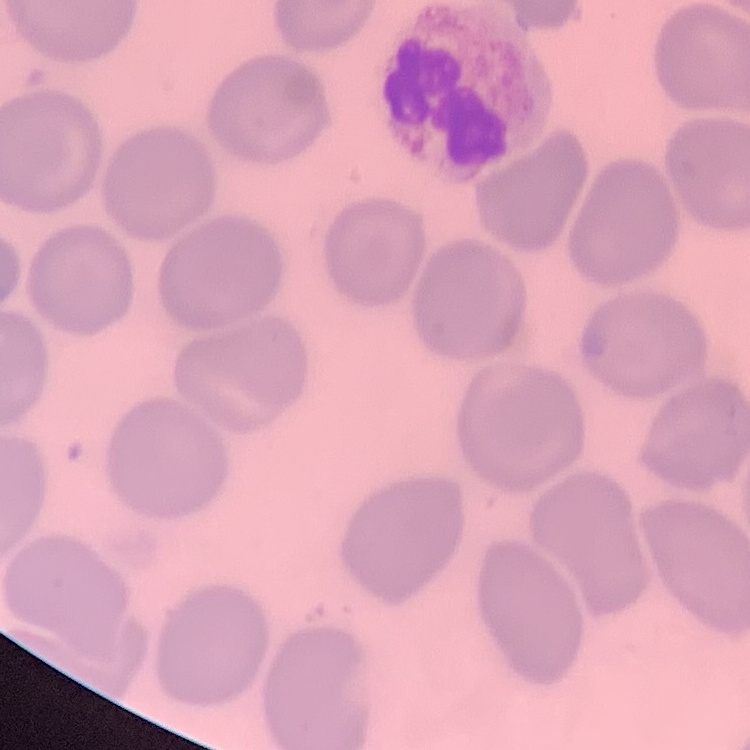

Summary:
  - Red blood cell morphology: no rouleaux formation
  - Preparation: thin peripheral smear
  - Stain: Field's or Giemsa
  - Image type: one tile cut from a larger photomicrograph